Report the malaria status of this cell.
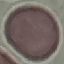

It is uninfected.

Giemsa stain. Acquired by smartphone through the microscope eyepiece. Thin blood film. Automatically extracted cell patch, resized to 64 × 64 pixels.